Identify the parasite.
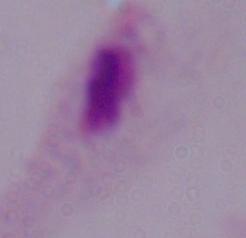

A trichomonad.

1000x magnification. Micrograph.